Report the malaria status of this cell.
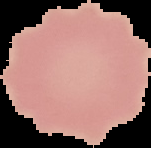

It is uninfected.

preparation = thin blood film
image type = segmented cell region with the area outside set to black
image size = 151×148 pixels